Identify the cell.
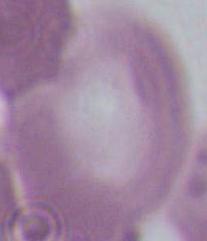
An erythrocyte.

Summary:
  - Modality: micrograph
  - Magnification: 1000x